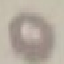
Malaria status: uninfected. Giemsa stain. Thin smear of blood. Automatically extracted cell patch, resized to 64 × 64 pixels. Acquired by smartphone through the microscope eyepiece.